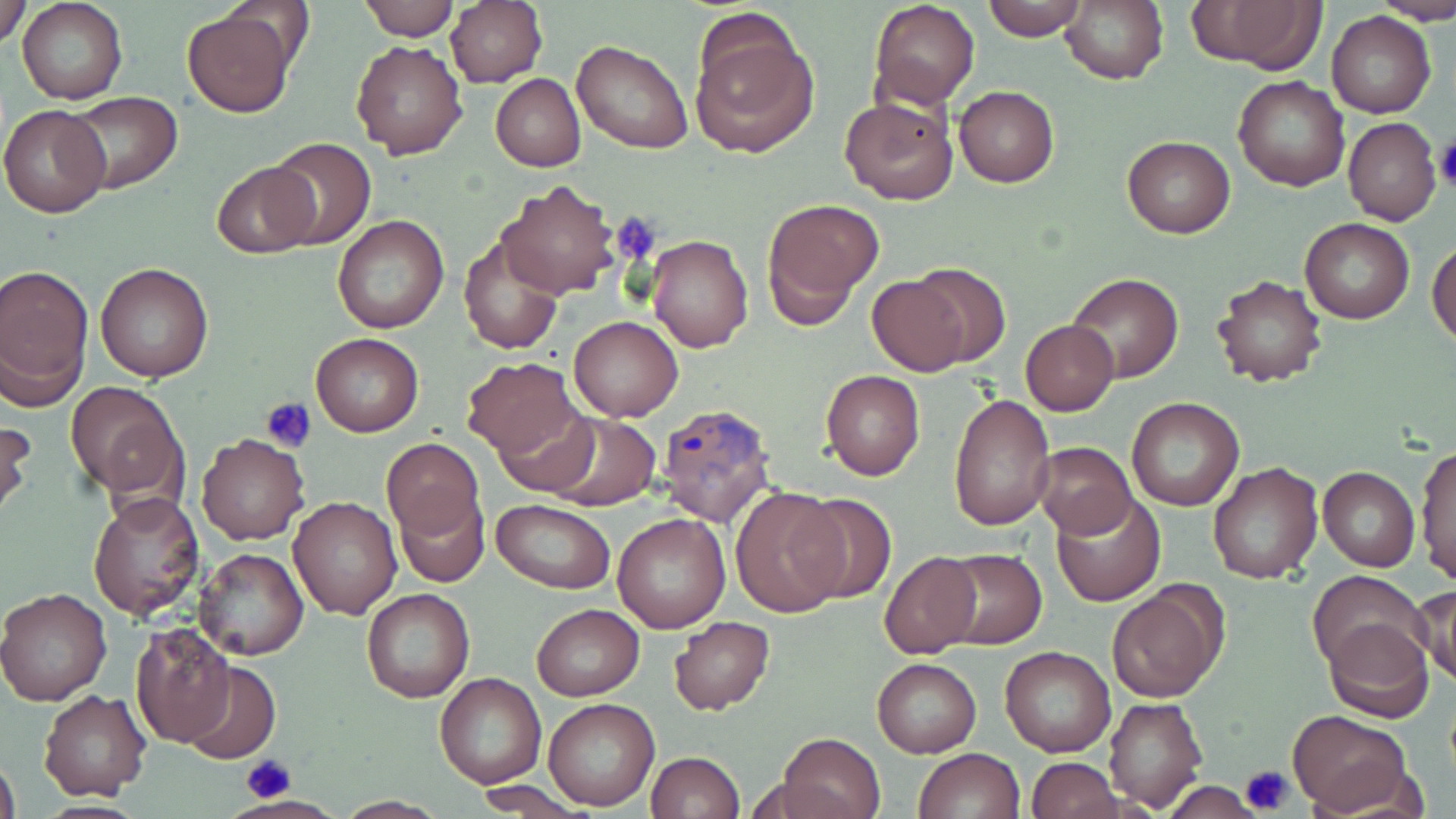

Approximate bounding boxes as (x1,y1)-(x2,y2) corner pairs in pixels. Uninfected red blood cell locations: (1,0)-(30,48), (18,0)-(127,104), (355,0)-(460,41), (446,0)-(547,89), (868,0)-(979,109), (980,0)-(1087,40), (1184,0)-(1326,74), (1376,0)-(1456,25), (1059,2)-(1168,85), (181,6)-(300,118), (1327,11)-(1436,119), (689,17)-(819,158), (349,38)-(468,159), (572,38)-(692,153), (491,74)-(585,171), (1233,75)-(1349,192), (953,85)-(1058,187), (63,90)-(184,196), (839,97)-(958,204), (1,104)-(111,219), (1342,116)-(1441,226), (1121,135)-(1235,238), (266,138)-(377,250), (211,162)-(320,256), (495,179)-(618,299), (761,197)-(884,325), (333,214)-(448,334), (1299,216)-(1414,325), (460,233)-(566,354), (646,235)-(754,354), (1429,239)-(1456,349), (95,262)-(214,382), (908,263)-(1012,368), (0,265)-(94,405), (1066,274)-(1183,383), (1211,275)-(1326,389), (867,277)-(967,375), (569,315)-(683,421), (1020,321)-(1118,417), (311,332)-(424,437), (461,358)-(580,459), (821,369)-(925,480), (69,382)-(184,499), (949,393)-(1055,531), (1126,397)-(1245,513), (493,405)-(602,496), (543,413)-(661,511), (0,417)-(34,525), (196,432)-(308,545), (382,439)-(484,538), (1031,441)-(1137,538), (1415,442)-(1456,586), (1207,461)-(1323,585), (1318,466)-(1420,571), (732,489)-(845,618), (88,490)-(204,621), (794,490)-(896,604), (1051,491)-(1165,607), (395,492)-(488,587), (290,496)-(401,619), (490,498)-(615,594), (613,512)-(731,634), (192,547)-(308,660), (938,547)-(1048,649), (879,550)-(983,659), (1307,570)-(1430,679), (1412,584)-(1456,687), (1107,585)-(1226,702), (0,586)-(112,706), (362,588)-(475,703), (530,604)-(645,701), (669,617)-(775,714), (1322,617)-(1433,722), (132,625)-(236,747), (1000,645)-(1116,757), (872,657)-(982,757), (180,659)-(281,764), (435,674)-(546,789), (39,689)-(151,803), (1103,696)-(1209,813), (544,697)-(659,811), (1289,709)-(1413,815), (778,733)-(887,819), (913,747)-(1024,819), (0,752)-(21,819), (646,752)-(745,819), (1026,756)-(1122,819), (467,780)-(590,814). Platelet locations: (1434,136)-(1456,193), (609,214)-(664,265), (262,396)-(318,451), (242,755)-(296,801), (1239,764)-(1297,814). Plasmodium ovale-infected red blood cell locations: (654,403)-(779,526). Slide-level diagnosis: Plasmodium ovale. Image is 1456×819 pixels. 1000x magnification. Single field of view. May-Grünwald-Giemsa-stained preparation. Light microscopy. Thin blood film.